State which parasite is depicted.
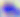

Toxoplasma gondii.

Summary:
  - Modality: micrograph
  - Magnification: 400x